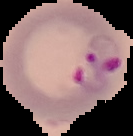 Image is 133×136 pixels. From a thin blood smear. The area outside the segmented cell region is set to black. Result: Plasmodium parasites identified.